Outline each blood parasite and name the species.
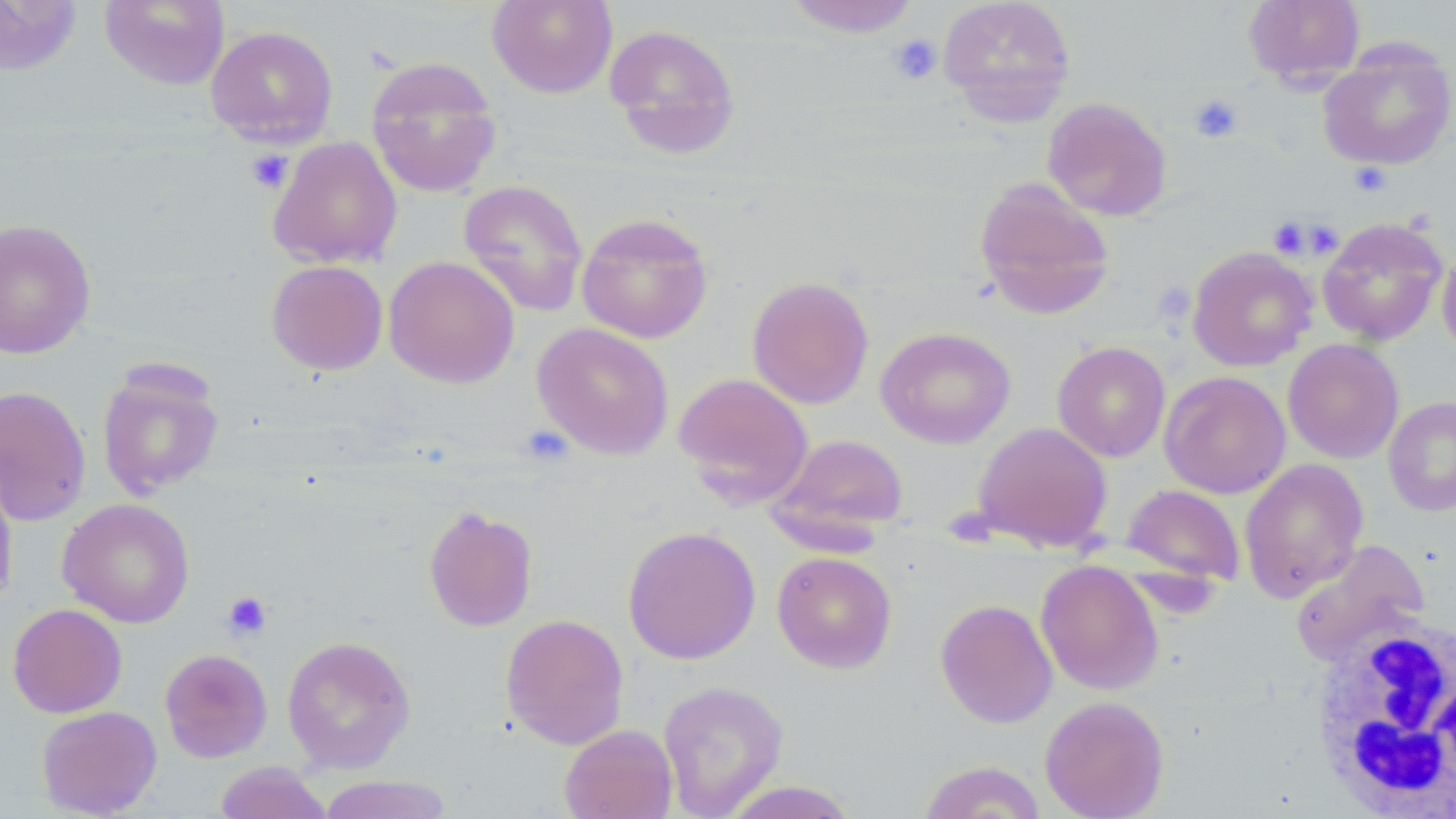

No blood parasites seen.

Summary:
  - Coordinate format: approximate bounding boxes as (x1, y1, x2, y2) in pixels
  - Uninfected red blood cell locations: (99, 0, 229, 90), (487, 0, 618, 99), (782, 0, 922, 37), (937, 0, 1077, 124), (1242, 0, 1366, 88), (0, 1, 81, 75), (604, 23, 741, 159), (205, 25, 339, 147), (1317, 42, 1456, 172), (365, 55, 503, 198), (1042, 97, 1173, 221), (267, 136, 402, 269), (973, 177, 1115, 319), (458, 179, 589, 318), (576, 212, 713, 343), (1317, 217, 1448, 346), (0, 218, 96, 359), (1187, 246, 1318, 371), (1437, 246, 1456, 359), (384, 255, 520, 388), (266, 259, 388, 376), (747, 277, 874, 409), (531, 322, 674, 460), (876, 326, 1016, 449), (1283, 339, 1404, 463), (1052, 341, 1171, 462), (96, 361, 225, 500), (673, 371, 814, 507), (1160, 371, 1290, 499), (0, 385, 91, 526), (1383, 396, 1456, 517), (973, 421, 1112, 551), (770, 433, 910, 537), (1240, 458, 1369, 601), (0, 466, 18, 612), (1121, 484, 1245, 588), (57, 498, 195, 628), (422, 504, 539, 632), (622, 526, 761, 665), (1290, 540, 1429, 663), (771, 551, 897, 673), (1036, 560, 1164, 695), (935, 598, 1058, 729), (7, 603, 127, 718), (499, 613, 630, 750), (282, 635, 416, 773), (160, 648, 273, 762), (658, 680, 789, 818), (1040, 695, 1169, 819), (36, 705, 162, 817), (559, 724, 678, 819), (918, 760, 1048, 818), (214, 761, 333, 819), (316, 775, 453, 819), (719, 781, 861, 818)
  - White blood cell locations: (1306, 613, 1455, 815)
  - Platelet locations: (886, 33, 942, 86), (1189, 94, 1244, 143), (245, 149, 292, 194), (1350, 162, 1392, 197), (1267, 217, 1312, 259), (519, 423, 573, 467), (221, 591, 272, 640)
  - Slide-level diagnosis: no evidence of blood parasites
  - Image size: 1456×819 pixels
  - Modality: optical microscopy
  - Magnification: 1000x
  - Stain: May-Grünwald-Giemsa
  - Field of view: single
  - Preparation: thin blood film